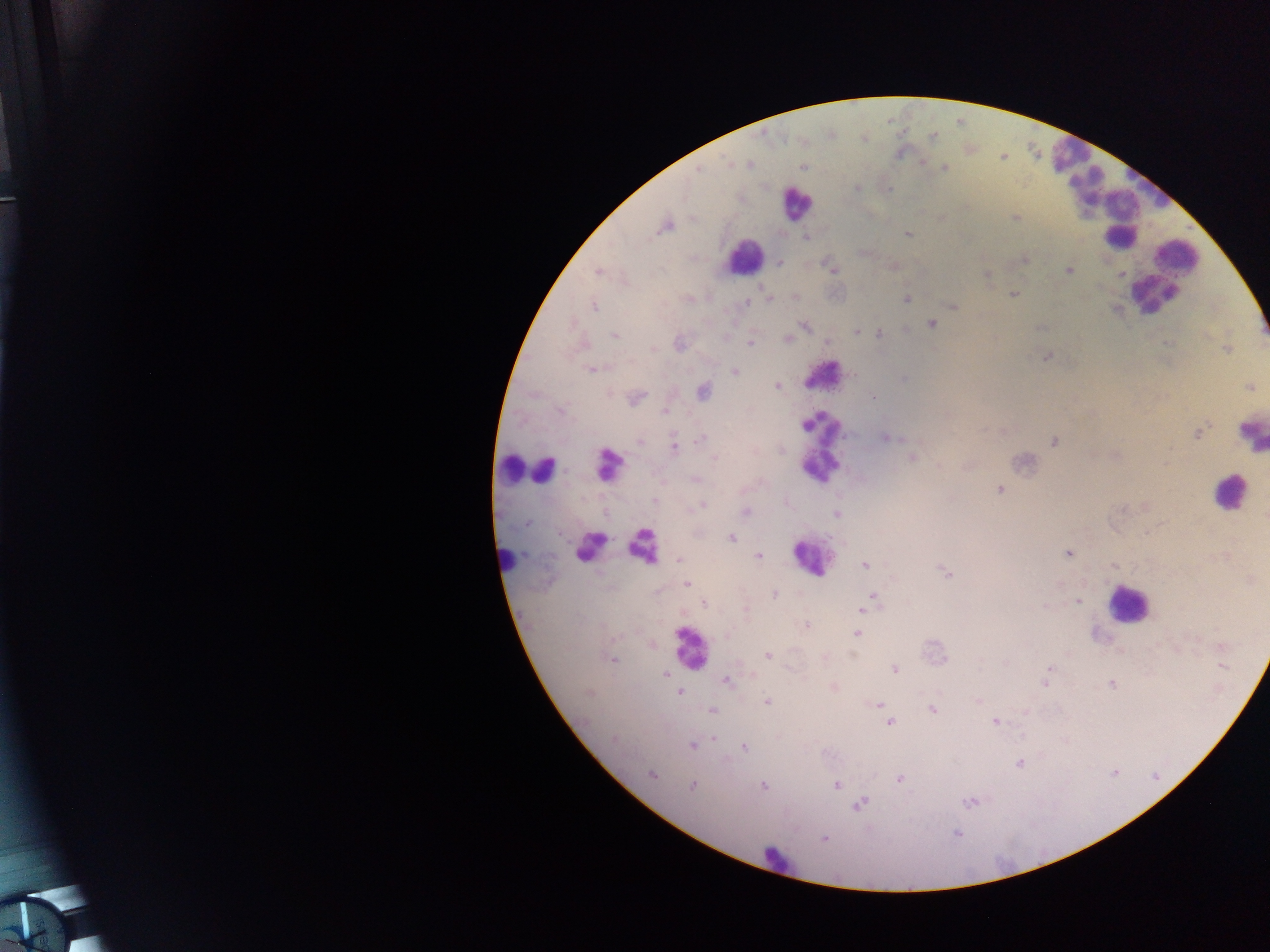

Approximate centers as (x, y) in pixels.
Summary:
  - Leukocyte locations (subset; some below the resolvable size): (1075, 168), (1136, 194), (795, 204), (1119, 236), (743, 255), (1180, 258), (1151, 295), (824, 375), (1250, 434), (819, 444), (608, 465), (512, 468), (543, 469), (1228, 493), (592, 545), (640, 546), (811, 558), (506, 559), (1126, 604), (689, 648), (780, 860)
  - Malaria parasite locations: (933, 136), (731, 164), (748, 165), (802, 166), (944, 168), (698, 170), (857, 188), (888, 189), (1015, 218), (666, 226), (909, 235), (806, 237), (1024, 260), (780, 263), (832, 269), (1069, 270), (598, 271), (987, 275), (1013, 295), (769, 298), (795, 298), (906, 299), (747, 303), (593, 306), (954, 306), (932, 324), (804, 326), (857, 332), (879, 333), (614, 335), (788, 339), (750, 342), (828, 343), (679, 344), (653, 349), (1227, 349), (1046, 357), (592, 369), (735, 372), (904, 378), (777, 386), (1248, 387), (701, 391), (635, 397), (873, 397), (561, 411), (665, 412), (1198, 433), (886, 437), (702, 438), (639, 442), (1054, 442), (674, 446), (912, 457), (714, 458), (695, 479), (999, 489), (655, 500), (701, 506), (745, 512), (836, 514), (527, 523), (731, 538), (1068, 553), (759, 556), (679, 559), (865, 564), (1115, 565), (946, 572), (687, 584), (774, 594), (874, 597), (1078, 601), (704, 604), (866, 606), (862, 609), (746, 611), (807, 625), (857, 634), (726, 636), (768, 655), (614, 659), (1223, 667), (1049, 668), (895, 669), (665, 673), (727, 682), (1045, 682), (1111, 684), (680, 691), (767, 702), (878, 705), (932, 709), (712, 711), (890, 722), (995, 722), (715, 737), (614, 738), (692, 745), (745, 747), (1019, 763), (652, 774), (900, 779), (836, 785), (692, 786), (764, 786), (969, 802), (861, 803), (956, 834), (824, 839)
  - Country: Ghana
  - Preparation: thick blood film
  - Image size: 1270×952 pixels
  - Field of view: single
  - Capture: mobile-phone photograph through a microscope